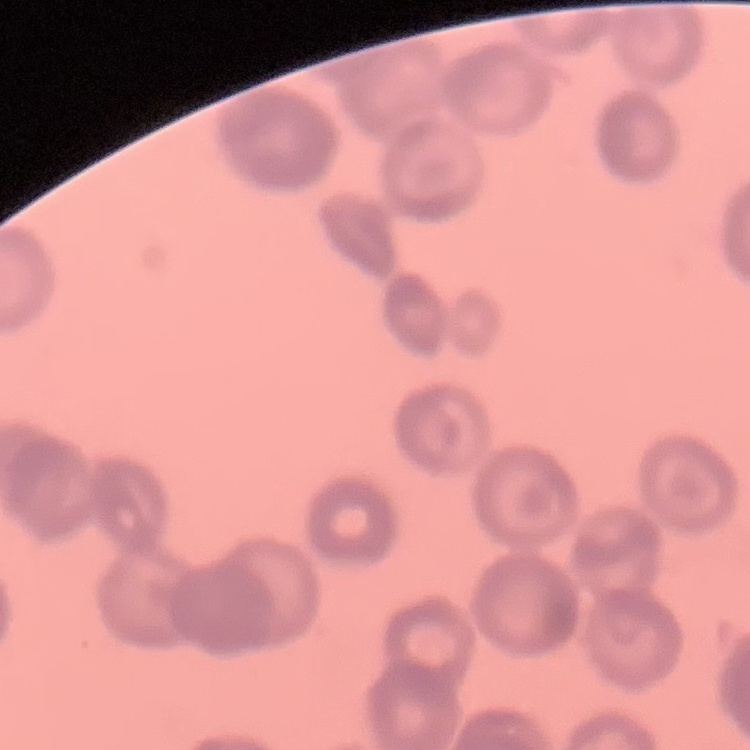

Summary:
  - Red blood cell morphology: rouleaux formation
  - Preparation: thin blood smear
  - Stain: Field's or Giemsa
  - Image type: one tile cut from a larger photomicrograph